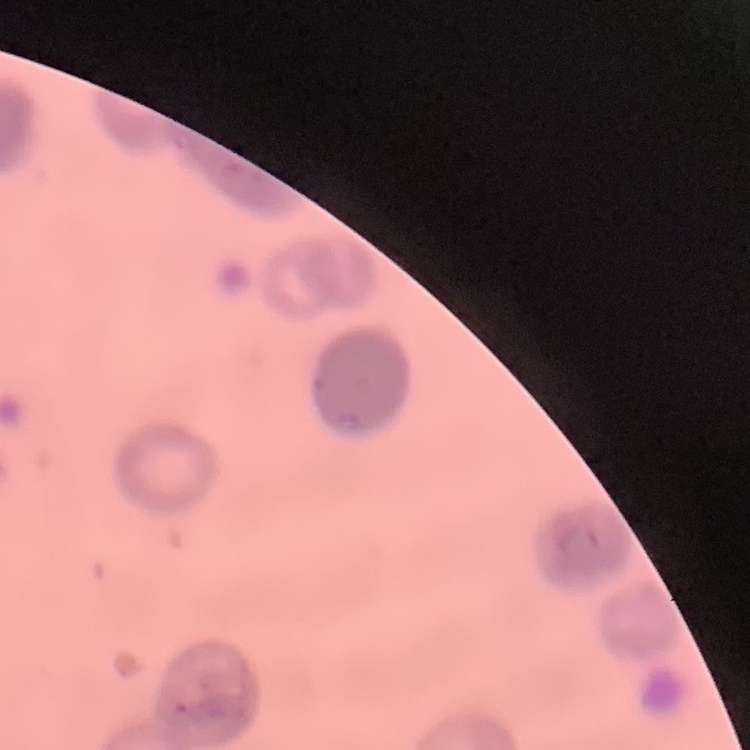 The red blood cells exhibit rouleaux formation. Thin blood smear. Square crop of a larger photomicrograph. Stained with either Field's or Giemsa.